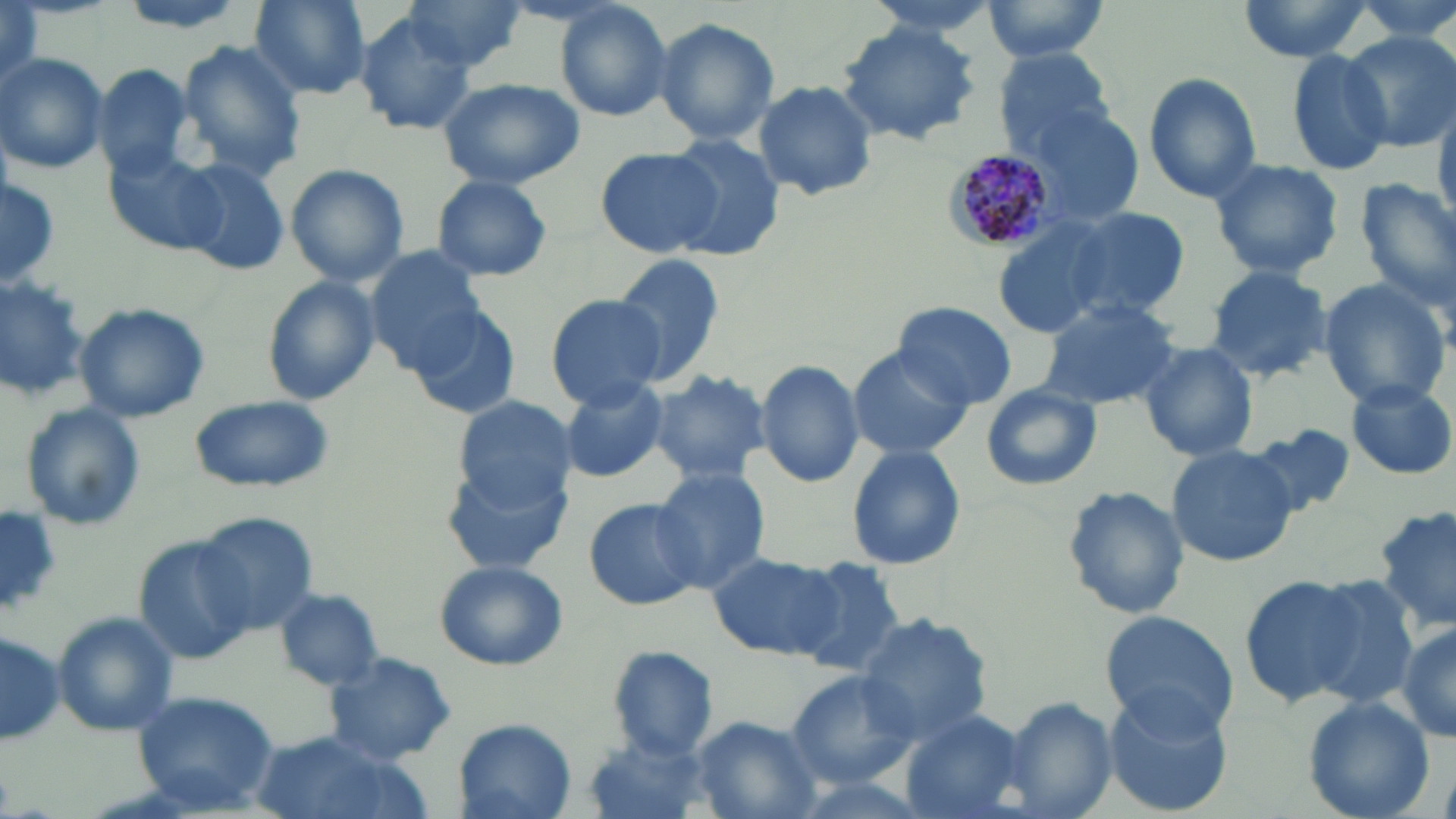

slide-level diagnosis = Plasmodium malariae
preparation = thin blood film
uninfected red blood cell locations = approximate bounding boxes as named x1/y1/x2/y2 corners in pixels: (x1=109, y1=0, x2=258, y2=34), (x1=249, y1=0, x2=371, y2=99), (x1=399, y1=0, x2=529, y2=77), (x1=855, y1=0, x2=1010, y2=40), (x1=981, y1=0, x2=1114, y2=62), (x1=1238, y1=0, x2=1371, y2=62), (x1=552, y1=1, x2=673, y2=122), (x1=2, y1=5, x2=42, y2=95), (x1=354, y1=13, x2=480, y2=136), (x1=655, y1=18, x2=779, y2=145), (x1=835, y1=21, x2=982, y2=146), (x1=1344, y1=30, x2=1455, y2=151), (x1=175, y1=41, x2=308, y2=180), (x1=993, y1=47, x2=1118, y2=158), (x1=1282, y1=48, x2=1394, y2=175), (x1=0, y1=53, x2=109, y2=175), (x1=93, y1=63, x2=195, y2=181), (x1=1142, y1=72, x2=1265, y2=201), (x1=438, y1=78, x2=585, y2=188), (x1=752, y1=80, x2=879, y2=202), (x1=1018, y1=102, x2=1145, y2=229), (x1=662, y1=137, x2=786, y2=259), (x1=593, y1=144, x2=724, y2=259), (x1=106, y1=150, x2=225, y2=257), (x1=1208, y1=158, x2=1346, y2=278), (x1=174, y1=159, x2=289, y2=276), (x1=287, y1=165, x2=408, y2=286), (x1=432, y1=175, x2=554, y2=281), (x1=0, y1=177, x2=60, y2=288), (x1=1354, y1=180, x2=1456, y2=309), (x1=1051, y1=206, x2=1192, y2=322), (x1=990, y1=214, x2=1139, y2=339), (x1=365, y1=248, x2=487, y2=373), (x1=612, y1=253, x2=726, y2=387), (x1=1203, y1=264, x2=1334, y2=384), (x1=0, y1=268, x2=90, y2=398), (x1=261, y1=276, x2=379, y2=406), (x1=1317, y1=279, x2=1452, y2=408), (x1=546, y1=295, x2=666, y2=409), (x1=1034, y1=298, x2=1180, y2=410), (x1=73, y1=302, x2=210, y2=423), (x1=892, y1=302, x2=1018, y2=411), (x1=409, y1=308, x2=518, y2=419), (x1=1132, y1=341, x2=1259, y2=463), (x1=846, y1=347, x2=974, y2=462), (x1=754, y1=357, x2=864, y2=488), (x1=648, y1=367, x2=772, y2=486), (x1=556, y1=376, x2=669, y2=483), (x1=1346, y1=380, x2=1455, y2=479), (x1=979, y1=384, x2=1102, y2=492), (x1=187, y1=395, x2=333, y2=493), (x1=453, y1=396, x2=577, y2=508), (x1=17, y1=402, x2=147, y2=534), (x1=1248, y1=425, x2=1357, y2=520), (x1=845, y1=445, x2=966, y2=571), (x1=1166, y1=445, x2=1298, y2=568), (x1=651, y1=466, x2=770, y2=590), (x1=1058, y1=486, x2=1190, y2=622), (x1=584, y1=498, x2=702, y2=612), (x1=1374, y1=503, x2=1456, y2=636), (x1=0, y1=510, x2=64, y2=616), (x1=194, y1=512, x2=321, y2=635), (x1=138, y1=538, x2=253, y2=664), (x1=706, y1=550, x2=843, y2=661), (x1=787, y1=556, x2=912, y2=677), (x1=434, y1=560, x2=567, y2=670), (x1=1238, y1=573, x2=1369, y2=708), (x1=1289, y1=573, x2=1423, y2=714), (x1=275, y1=587, x2=385, y2=691), (x1=51, y1=611, x2=181, y2=736), (x1=1098, y1=611, x2=1240, y2=739), (x1=854, y1=613, x2=992, y2=746), (x1=1395, y1=622, x2=1456, y2=744), (x1=0, y1=630, x2=65, y2=748), (x1=607, y1=645, x2=718, y2=759), (x1=324, y1=652, x2=457, y2=766), (x1=786, y1=671, x2=921, y2=786), (x1=1099, y1=687, x2=1237, y2=817), (x1=132, y1=690, x2=281, y2=815), (x1=1000, y1=695, x2=1117, y2=819), (x1=1302, y1=697, x2=1435, y2=819), (x1=898, y1=710, x2=1029, y2=819), (x1=688, y1=716, x2=824, y2=817), (x1=450, y1=718, x2=578, y2=819), (x1=245, y1=733, x2=420, y2=819), (x1=586, y1=736, x2=713, y2=819)
field of view = one of a larger specimen
Plasmodium malariae-infected red blood cell locations = approximate bounding boxes as named x1/y1/x2/y2 corners in pixels: (x1=942, y1=150, x2=1055, y2=252)
modality = optical microscopy
magnification = 1000x
stain = May-Grünwald-Giemsa
image size = 1456×819 pixels